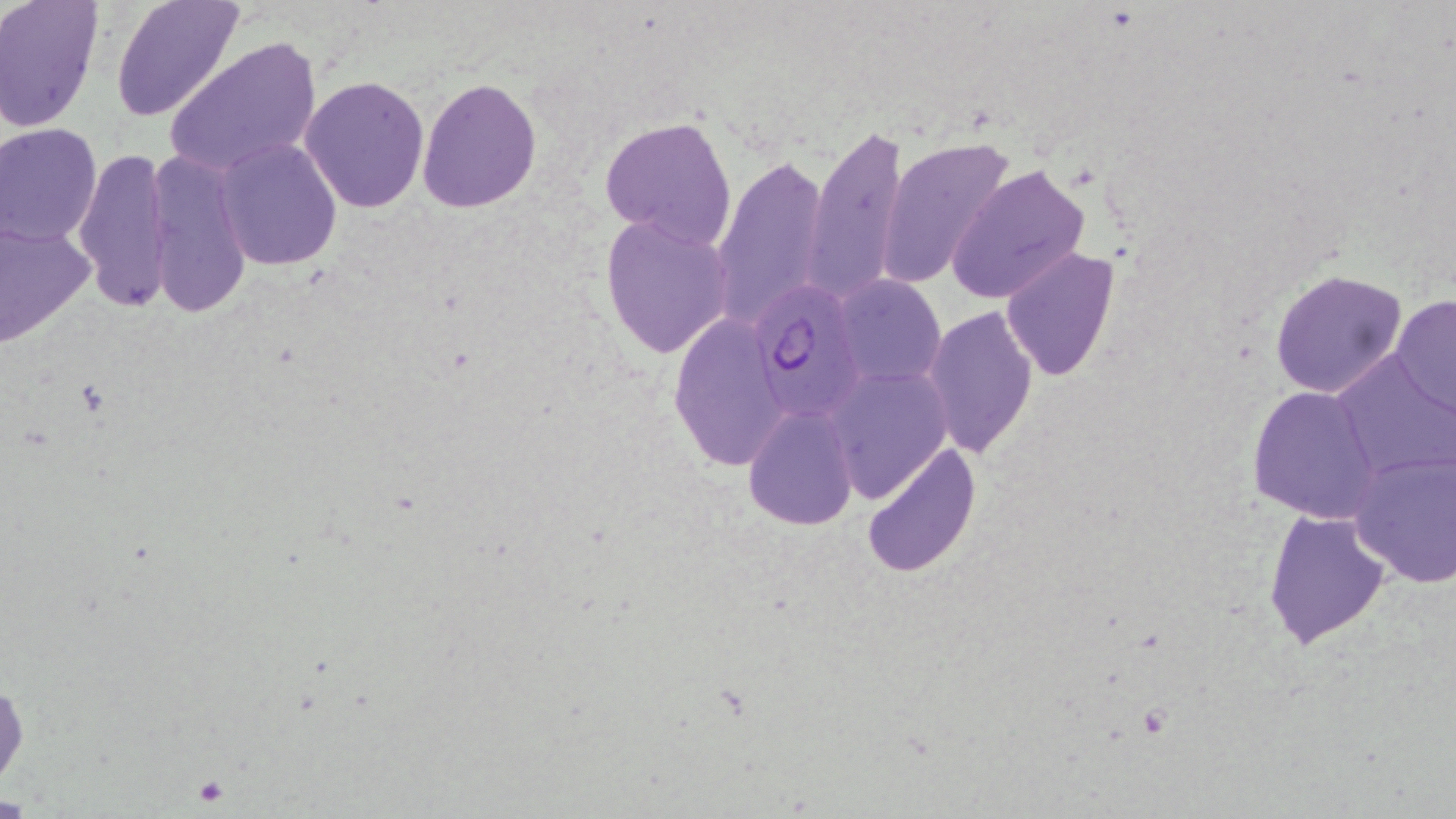
Approximate bounding boxes as (x1,y1)-(x2,y2) corner pairs in pixels. Platelet locations: (194,777)-(229,808). Uninfected red blood cell locations: (0,0)-(103,131), (109,0)-(246,124), (166,36)-(321,180), (300,76)-(431,214), (417,77)-(543,211), (599,115)-(737,249), (0,122)-(104,248), (805,122)-(909,298), (875,134)-(1016,289), (215,139)-(343,271), (74,146)-(177,313), (145,150)-(252,320), (713,153)-(830,328), (947,163)-(1093,306), (600,214)-(734,359), (0,216)-(97,350), (1001,246)-(1121,381), (1269,267)-(1408,398), (835,273)-(946,386), (1390,295)-(1455,419), (922,303)-(1037,459), (668,311)-(791,472), (1331,349)-(1456,481), (825,365)-(954,500), (1247,384)-(1383,524), (741,404)-(859,530), (861,440)-(981,578), (1347,450)-(1456,588), (1262,507)-(1391,649), (0,678)-(26,791). Plasmodium falciparum-infected red blood cell locations: (754,280)-(865,421). Slide-level diagnosis: Plasmodium falciparum. Optical microscopy. May-Grünwald-Giemsa stain. Image is 1456×819 pixels. Thin blood film. Single field of view. Captured at 1000x magnification.